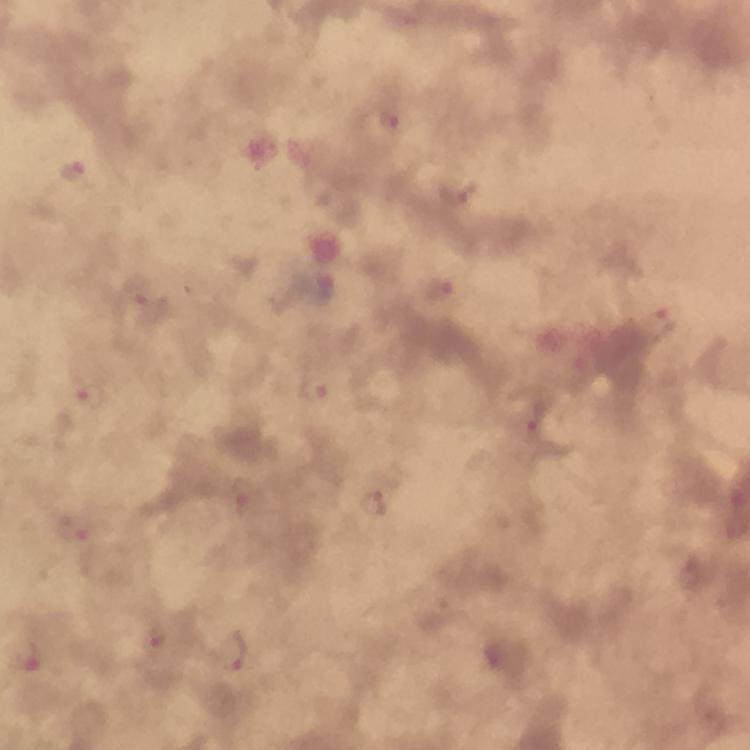

Approximate centers as (x, y) in pixels.
Summary:
  - Malaria parasite locations: (386, 124), (74, 171), (438, 290), (146, 303), (659, 322), (313, 389), (88, 396), (529, 428), (372, 504), (76, 529), (159, 639), (232, 653), (29, 661)
  - Stain: Giemsa
  - Immersion oil: applied
  - Magnification: 100x
  - Capture: smartphone mounted on the microscope
  - Cropped from: a single field of view
  - Image size: 750×750 pixels
  - Context: from a malaria diagnostic workup
  - Preparation: thick blood smear